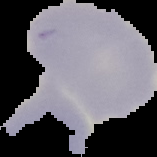
image_size: 157×157 pixels
preparation: thin blood film
result: negative for malaria parasites
image_type: cell region segmented out of the field of view; surrounding area masked to black